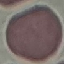

Malaria status: uninfected. Giemsa-stained preparation. Automatically extracted cell patch, resized to 64 × 64 pixels. Thin blood smear. Photographed with a smartphone camera at the microscope eyepiece.